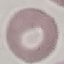
Malaria status: uninfected. Photographed with a smartphone camera at the microscope eyepiece. Cell patch, automatically extracted from a larger field of view and resized to 64 × 64 pixels. Giemsa stain. Thin smear of blood.